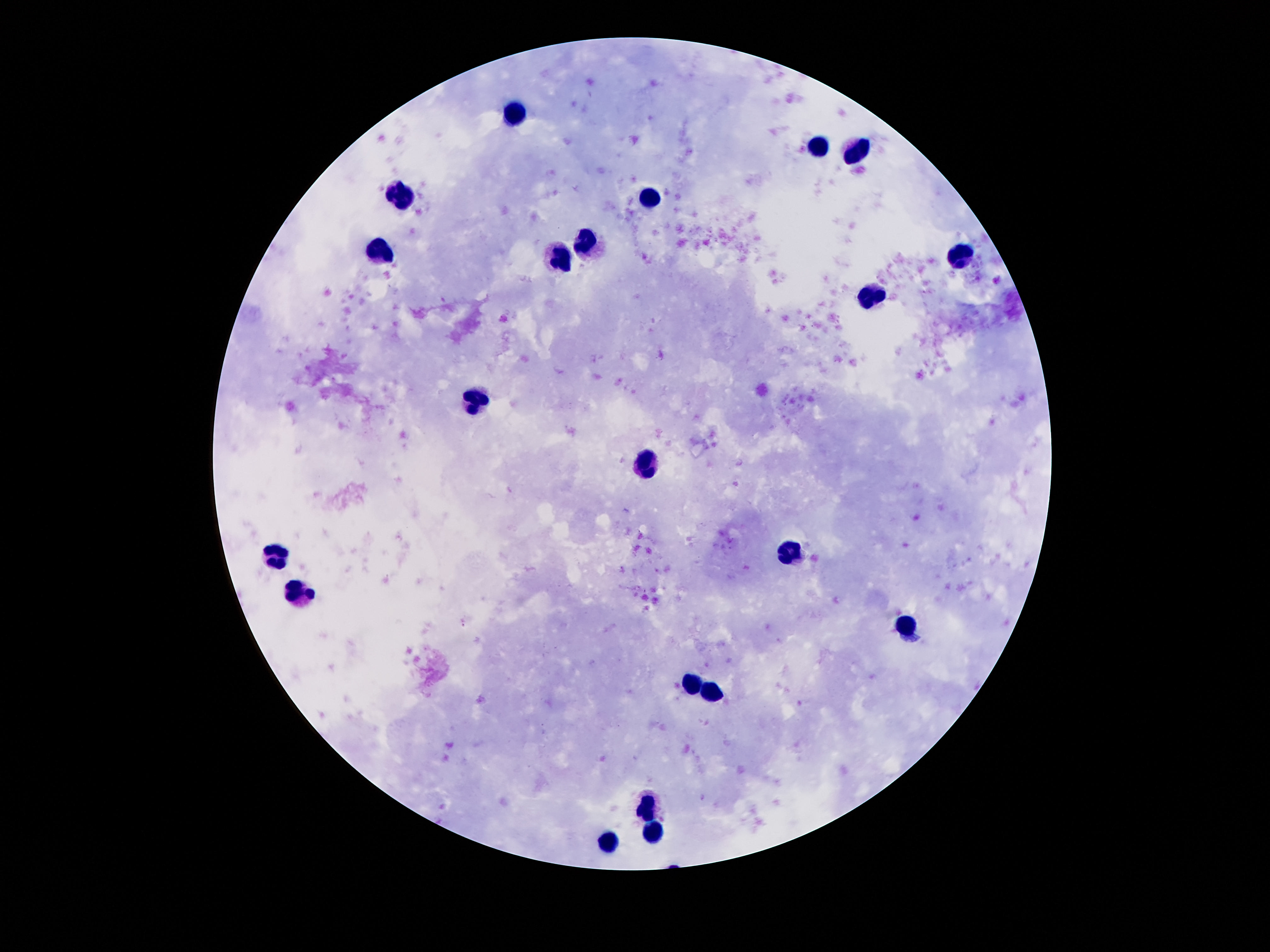
Approximate centers as {x, y} in pixels.
Summary:
  - Leukocyte locations: {517, 113}, {816, 146}, {861, 153}, {404, 196}, {652, 197}, {585, 241}, {382, 252}, {960, 256}, {562, 257}, {873, 294}, {476, 400}, {646, 463}, {790, 551}, {275, 554}, {302, 593}, {910, 626}, {693, 683}, {714, 691}, {648, 804}, {656, 826}, {609, 841}
  - Stain: Giemsa
  - Magnification: 100x
  - Image size: 1270×952 pixels
  - Field of view: one from this slide
  - Capture: smartphone camera through the microscope eyepiece
  - Preparation: thick blood smear
  - Patient malaria status: not infected